Assess this cell for malaria.
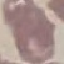
Uninfected.

{
  "stain": "Giemsa",
  "image_type": "automatically extracted cell patch, resized to 64 × 64 pixels",
  "preparation": "thin smear",
  "capture": "smartphone through the microscope eyepiece"
}